Comment on the morphology of the red blood cells.
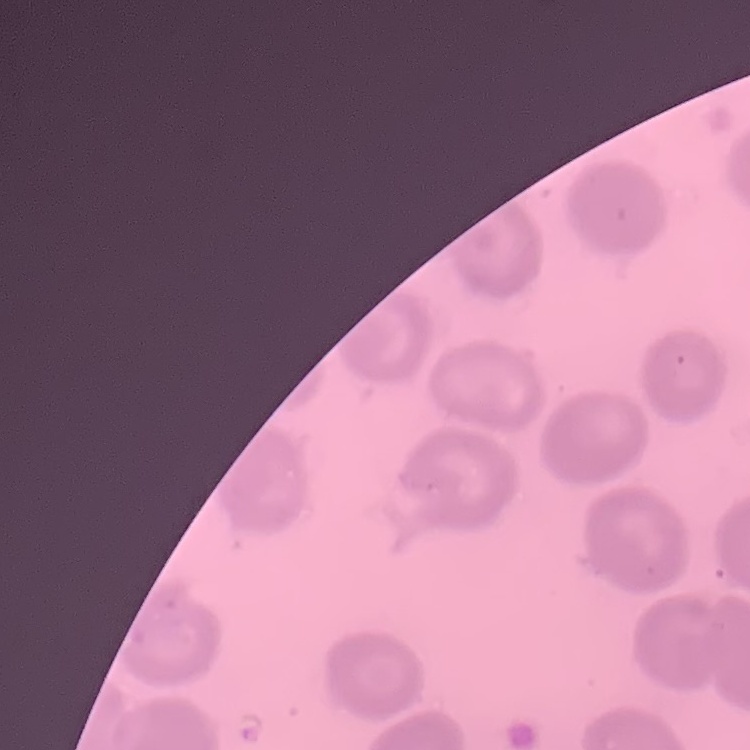
No rouleaux formation.

Summary:
  - Image type: square crop of a larger photomicrograph
  - Preparation: thin blood smear
  - Stain: Field's or Giemsa